Give the extent of all Plasmodium malariae-infected red blood cells.
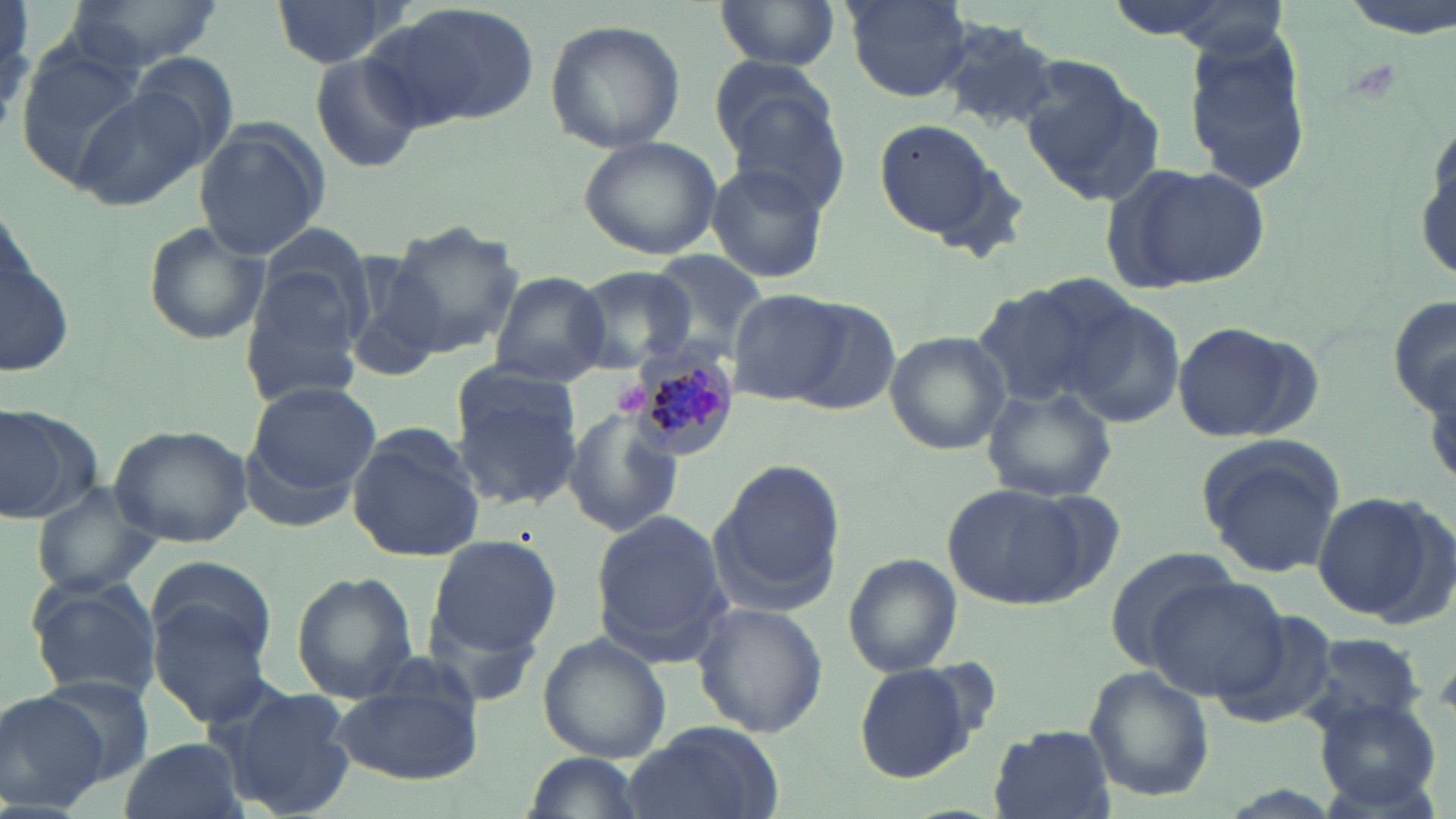
Approximate bounding boxes as (x1,y1)-(x2,y2) corner pairs in pixels.
Plasmodium malariae-infected red blood cells: (627,351)-(740,459).

{
  "slide_level_diagnosis": "Plasmodium malariae",
  "field_of_view": "one of a larger specimen",
  "stain": "May-Grünwald-Giemsa",
  "magnification": "1000x",
  "uninfected_red_blood_cell_locations": "approximate bounding boxes as (x1,y1)-(x2,y2) corner pairs in pixels: (54,0)-(220,73), (272,0)-(403,70), (713,0)-(844,76), (841,0)-(975,102), (380,2)-(540,127), (933,18)-(1065,133), (543,20)-(686,154), (1184,31)-(1314,191), (14,42)-(149,183), (309,50)-(428,174), (1019,60)-(1160,203), (722,73)-(845,209), (76,87)-(210,212), (875,119)-(1006,245), (193,120)-(330,257), (1415,135)-(1454,283), (579,136)-(723,260), (1106,162)-(1270,294), (705,163)-(830,286), (1,211)-(78,388), (142,221)-(270,345), (384,225)-(522,359), (333,251)-(449,384), (647,252)-(768,350), (242,265)-(367,402), (572,267)-(698,374), (488,271)-(611,388), (974,283)-(1109,404), (1389,288)-(1456,423), (730,290)-(847,406), (1064,299)-(1187,430), (788,300)-(902,416), (1173,322)-(1296,440), (885,331)-(1012,457), (450,366)-(585,508), (244,381)-(381,506), (981,385)-(1116,502), (0,404)-(99,526), (565,406)-(684,540), (106,424)-(252,549), (344,429)-(483,562), (1195,436)-(1349,580), (706,462)-(848,611), (30,482)-(162,597), (947,482)-(1094,610), (1314,491)-(1445,623), (590,511)-(735,662), (425,533)-(562,664), (1104,549)-(1243,667), (842,554)-(961,677), (147,555)-(277,661), (293,573)-(416,701), (25,576)-(162,703), (1143,577)-(1288,701), (150,597)-(275,726), (692,603)-(827,738), (1298,632)-(1431,734), (538,634)-(672,763), (851,662)-(988,786), (1085,665)-(1214,803), (328,666)-(485,784), (36,674)-(153,786), (216,684)-(358,818), (0,689)-(112,814), (1313,697)-(1443,811), (623,722)-(785,819), (985,726)-(1116,819), (117,737)-(248,819), (518,751)-(644,818)",
  "image_size": "1456×819 pixels",
  "preparation": "thin blood film",
  "platelet_locations": "approximate bounding boxes as (x1,y1)-(x2,y2) corner pairs in pixels: (614,382)-(650,415)",
  "modality": "optical microscopy"
}